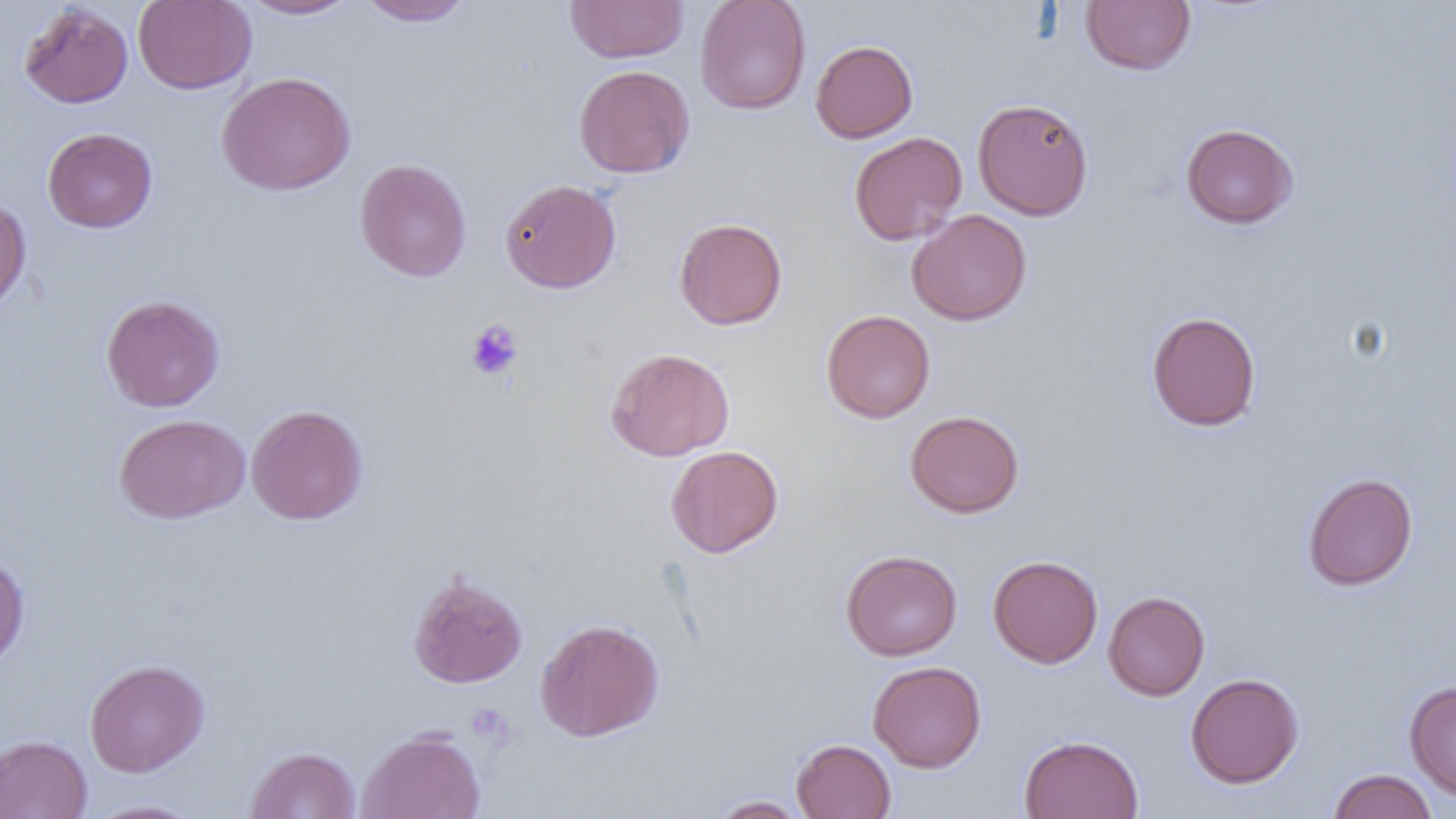
Approximate bounding boxes as (x1,y1)-(x2,y2) corner pairs in pixels. Uninfected red blood cell locations: (133,0)-(256,94), (238,0)-(359,20), (564,0)-(690,64), (695,0)-(811,115), (1081,0)-(1195,75), (358,1)-(475,27), (18,2)-(134,109), (810,40)-(918,143), (574,64)-(695,179), (216,71)-(356,195), (972,97)-(1094,220), (1180,123)-(1299,229), (42,127)-(157,233), (849,131)-(967,246), (354,159)-(471,282), (499,178)-(621,294), (0,196)-(32,316), (906,209)-(1032,325), (674,217)-(788,330), (101,294)-(225,412), (821,309)-(936,423), (1146,311)-(1261,432), (605,347)-(735,462), (246,403)-(369,526), (905,409)-(1025,518), (114,414)-(250,524), (665,445)-(784,558), (1302,472)-(1418,591), (840,549)-(963,661), (0,554)-(30,673), (988,554)-(1103,668), (408,572)-(527,689), (1103,591)-(1210,701), (535,618)-(664,742), (85,659)-(210,777), (867,661)-(986,773), (1186,672)-(1304,789), (1404,680)-(1456,800), (357,727)-(486,819), (0,734)-(92,819), (1019,734)-(1144,819), (790,738)-(897,819), (245,746)-(360,818), (1327,769)-(1437,819), (708,795)-(810,818), (84,798)-(206,819). Platelet locations: (466,319)-(523,381). Slide-level diagnosis: no evidence of blood parasites. Optical microscopy. Image is 1456×819 pixels. Single field of view. Thin blood smear. Captured at 1000x magnification.